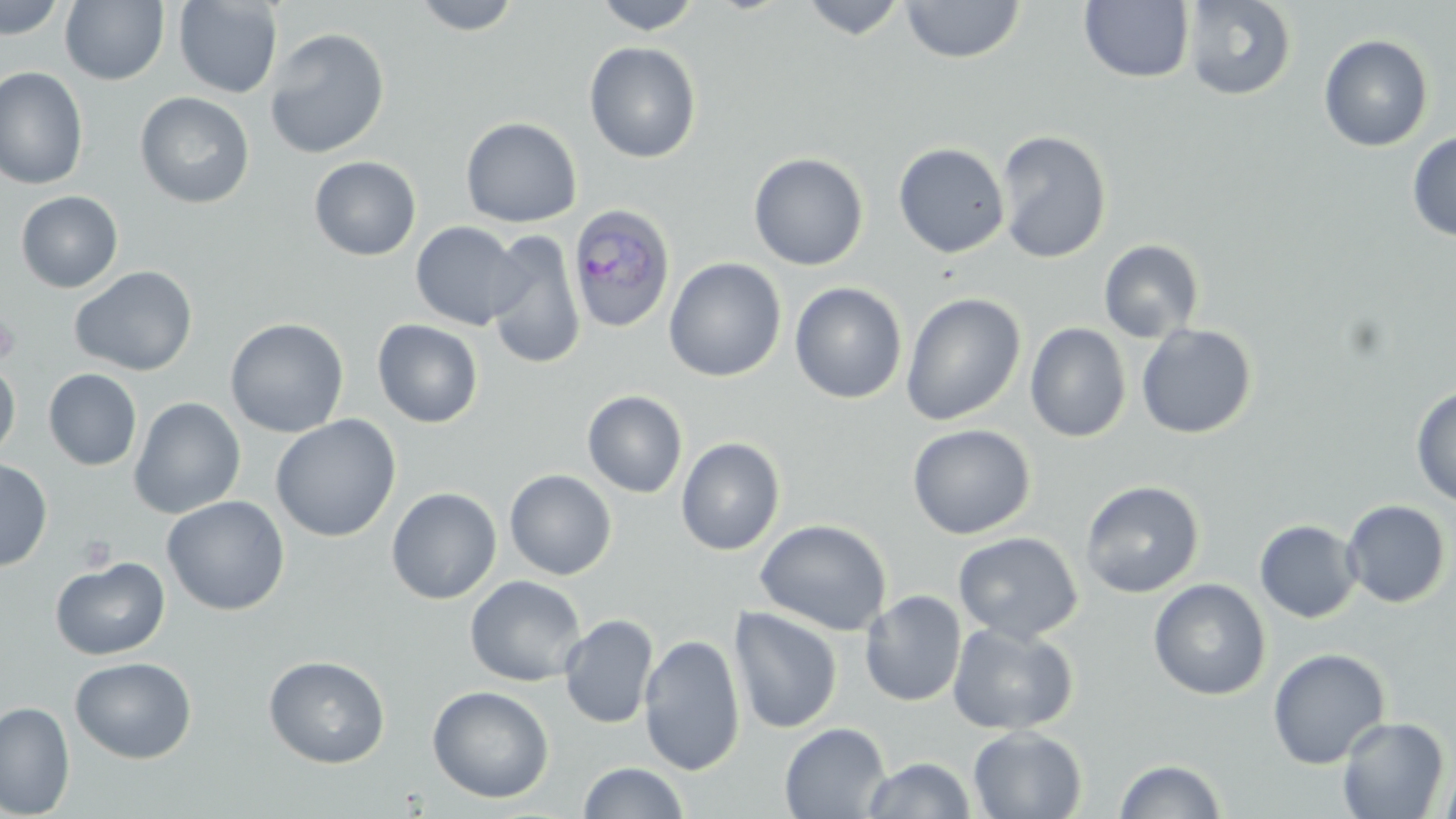
Approximate bounding boxes as [x1, y1, x2, y2] in pixels. Platelet locations: [0, 310, 20, 366], [77, 533, 117, 572]. Uninfected red blood cell locations: [0, 0, 68, 40], [59, 0, 169, 86], [173, 0, 282, 99], [411, 0, 522, 36], [593, 0, 703, 34], [799, 0, 909, 40], [1183, 0, 1296, 101], [901, 1, 1025, 63], [1079, 1, 1195, 84], [264, 27, 390, 159], [1319, 34, 1433, 152], [584, 41, 702, 163], [0, 67, 89, 190], [135, 92, 255, 209], [473, 116, 583, 351], [460, 117, 582, 227], [995, 129, 1112, 263], [1407, 131, 1456, 242], [893, 142, 1010, 258], [748, 152, 869, 270], [308, 155, 422, 261], [15, 190, 124, 293], [410, 221, 526, 331], [485, 229, 586, 370], [1099, 239, 1205, 343], [663, 257, 787, 383], [70, 265, 198, 377], [790, 282, 907, 404], [901, 292, 1026, 426], [224, 317, 349, 438], [372, 319, 483, 428], [1025, 322, 1132, 443], [1136, 323, 1257, 439], [0, 358, 21, 463], [43, 368, 142, 471], [1410, 386, 1456, 509], [582, 390, 688, 498], [128, 397, 246, 518], [270, 414, 401, 542], [907, 423, 1035, 540], [676, 437, 786, 556], [0, 458, 53, 571], [504, 469, 617, 580], [1080, 479, 1205, 598], [386, 487, 502, 604], [162, 495, 290, 615], [1341, 499, 1452, 608], [755, 518, 892, 636], [1255, 519, 1363, 623], [953, 531, 1083, 644], [50, 557, 170, 660], [465, 576, 587, 686], [1148, 578, 1271, 701], [860, 589, 967, 707], [728, 606, 843, 735], [559, 614, 659, 729], [947, 622, 1079, 735], [638, 633, 746, 775], [1268, 648, 1391, 769], [264, 655, 390, 768], [70, 656, 197, 764], [427, 685, 554, 804], [0, 700, 75, 818], [1336, 715, 1450, 819], [779, 722, 891, 818], [968, 726, 1087, 818], [864, 757, 976, 818], [1113, 758, 1228, 818], [1438, 761, 1456, 819], [577, 762, 689, 819]. Plasmodium ovale-infected red blood cell locations: [567, 203, 676, 334]. Slide-level diagnosis: Plasmodium ovale. Thin blood smear. Single field of view. Captured at 1000x magnification. Light microscopy. Image is 1456×819 pixels. May-Grünwald-Giemsa-stained preparation.